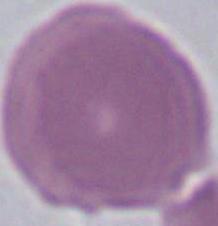

Summary:
  - Identification: red blood cell
  - Magnification: 1000x
  - Modality: photomicrograph